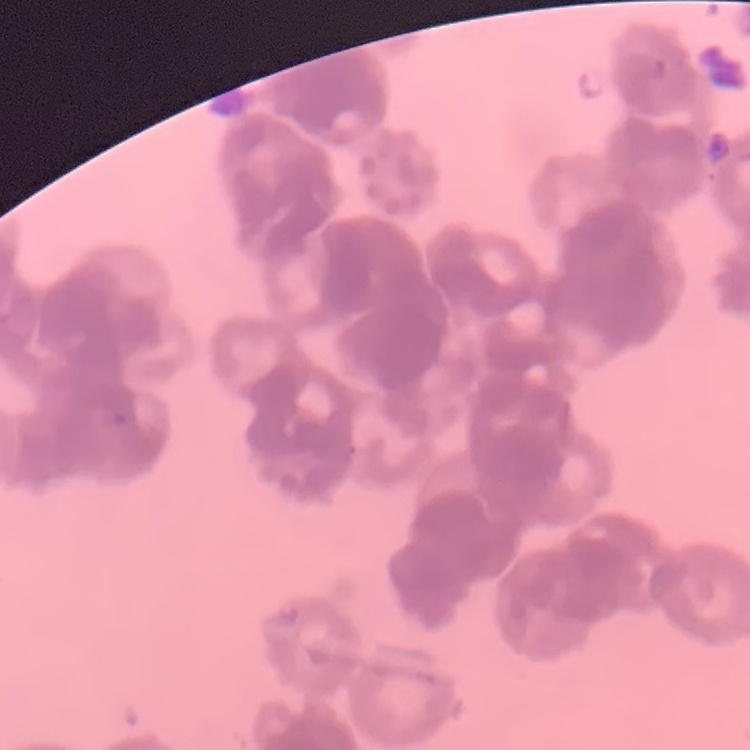 The erythrocytes show rouleaux formation. Thin peripheral smear. One tile cut from a larger photomicrograph. Field's or Giemsa stain.